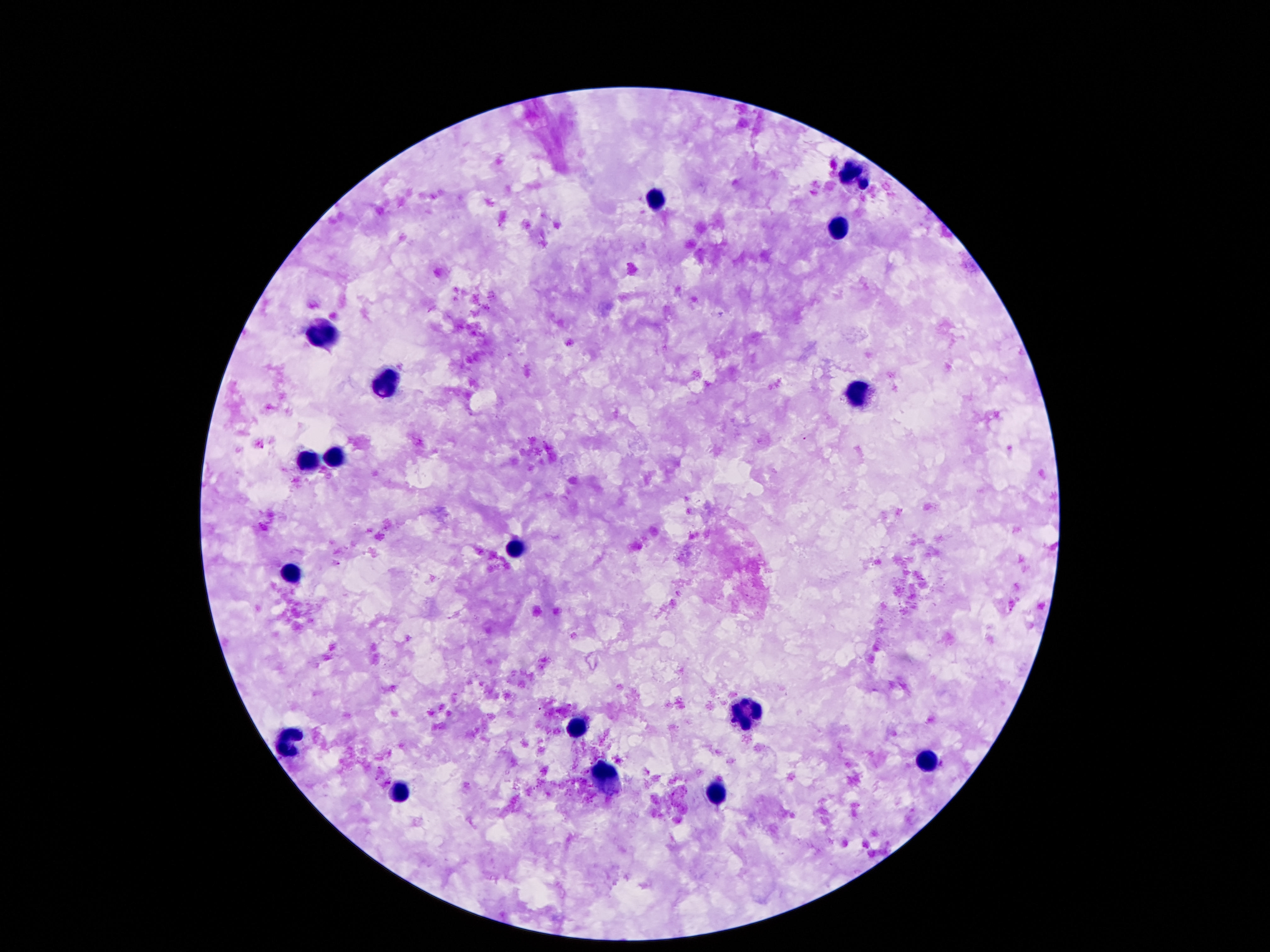

Approximate centers as [x, y] in pixels.
Summary:
  - Leukocyte locations: [856, 173], [655, 197], [839, 226], [323, 334], [384, 382], [858, 394], [337, 455], [307, 459], [514, 551], [294, 574], [749, 711], [579, 725], [288, 739], [925, 757], [612, 776], [718, 790], [397, 794]
  - Stain: Giemsa
  - Magnification: 100x
  - Capture: smartphone camera through the microscope eyepiece
  - Patient malaria status: not infected
  - Preparation: thick blood smear
  - Image size: 1270×952 pixels
  - Field of view: one from this slide